Report the malaria status of this cell.
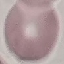

Uninfected.

stain = Giemsa
preparation = thin blood film
capture = smartphone camera at the microscope eyepiece
image type = cell patch, automatically extracted from a larger field of view and resized to 64 × 64 pixels